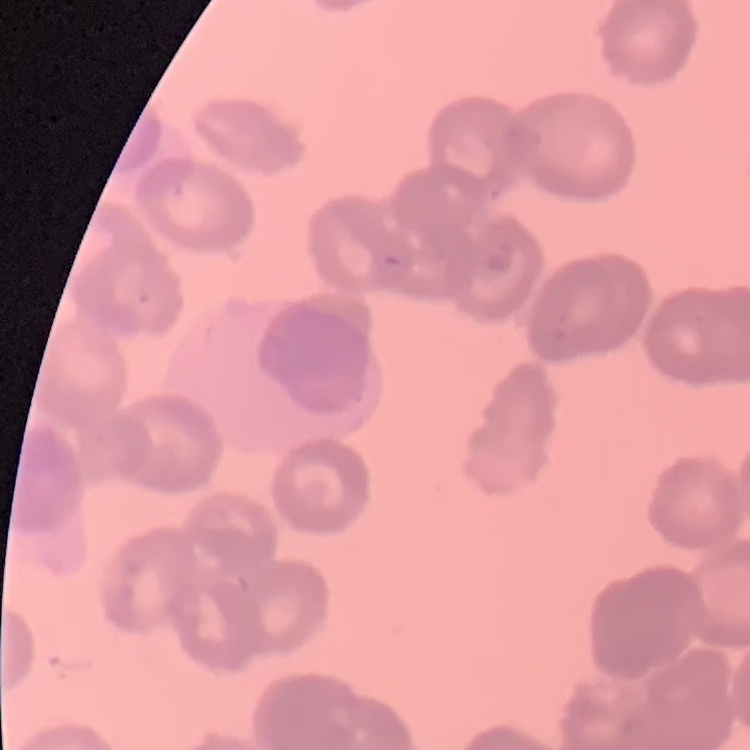
{
  "red_blood_cell_morphology": "rouleaux formation",
  "stain": "Field's or Giemsa",
  "preparation": "thin blood smear",
  "image_type": "one tile cut from a larger photomicrograph"
}